Report the malaria status of this cell.
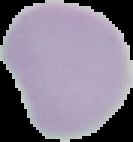

It is uninfected.

Segmented cell region on a black background. Image is 133×142 pixels. From a thin blood smear.